Classify this cell by malaria status.
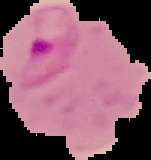

It is parasitized.

preparation = thin blood smear
image type = segmented cell region on a black background
image size = 151×160 pixels